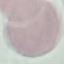
Malaria status: uninfected. Thin smear of blood. Automatically extracted cell patch, resized to 64 × 64 pixels. Giemsa-stained preparation. Acquired by smartphone through the microscope eyepiece.